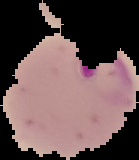
Summary:
  - Result: Plasmodium parasites identified
  - Preparation: thin blood film
  - Image size: 139×160 pixels
  - Image type: segmented cell region with the area outside set to black